Identify the blood parasite species.
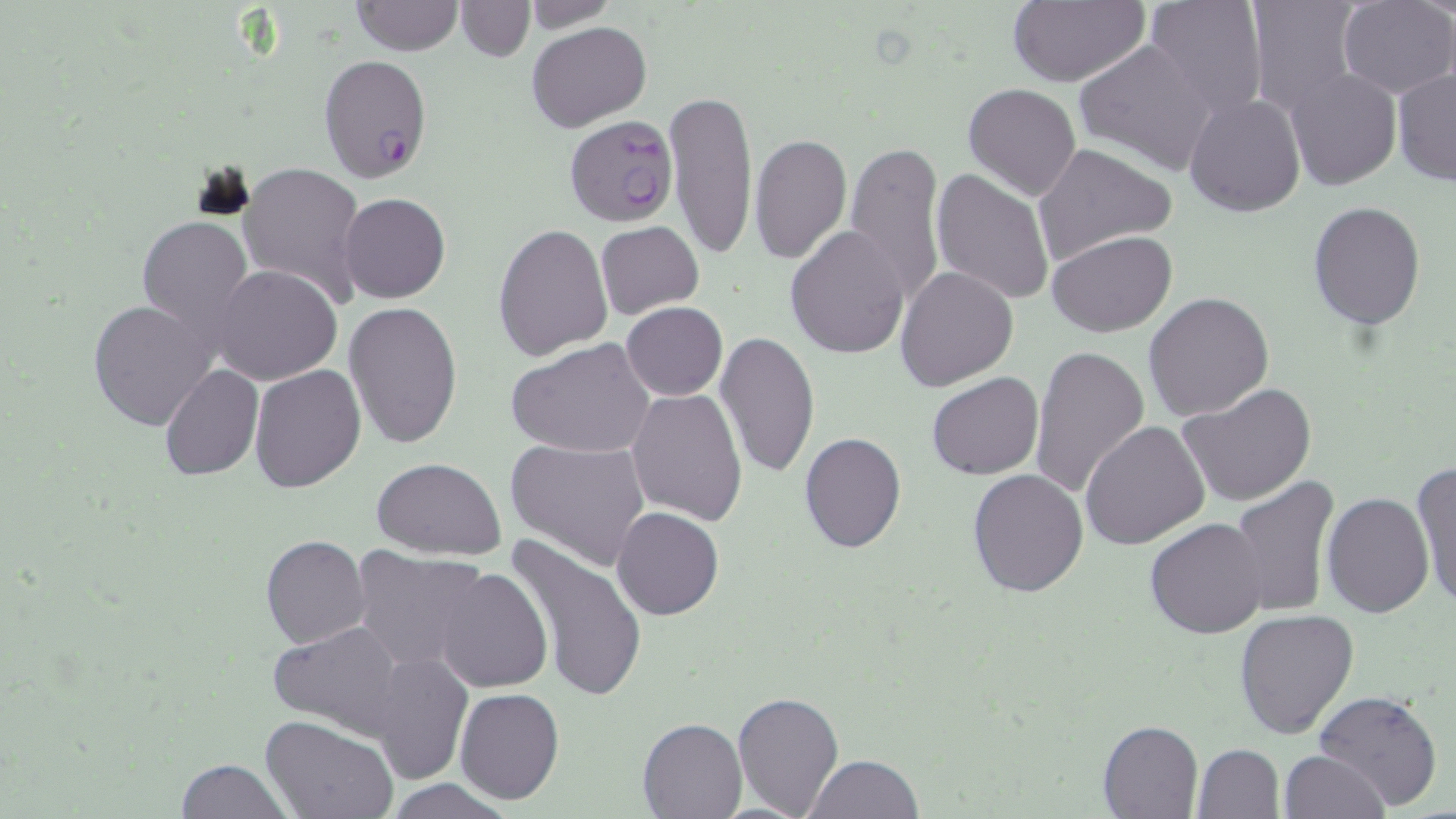

Plasmodium falciparum.

Summary:
  - Coordinate format: approximate bounding boxes as named x1/y1/x2/y2 corners in pixels
  - Uninfected red blood cell locations: (x1=454, y1=0, x2=535, y2=61), (x1=522, y1=0, x2=618, y2=33), (x1=1006, y1=0, x2=1150, y2=87), (x1=1143, y1=0, x2=1270, y2=118), (x1=1245, y1=0, x2=1362, y2=115), (x1=1337, y1=0, x2=1455, y2=98), (x1=351, y1=1, x2=463, y2=55), (x1=527, y1=20, x2=651, y2=131), (x1=1074, y1=38, x2=1219, y2=178), (x1=1286, y1=68, x2=1400, y2=190), (x1=1392, y1=69, x2=1456, y2=188), (x1=963, y1=82, x2=1081, y2=201), (x1=664, y1=88, x2=758, y2=259), (x1=1184, y1=93, x2=1307, y2=218), (x1=750, y1=131, x2=852, y2=265), (x1=845, y1=141, x2=944, y2=307), (x1=1032, y1=143, x2=1176, y2=269), (x1=237, y1=161, x2=366, y2=308), (x1=930, y1=169, x2=1055, y2=305), (x1=340, y1=193, x2=450, y2=302), (x1=1307, y1=201, x2=1426, y2=328), (x1=136, y1=213, x2=254, y2=351), (x1=595, y1=222, x2=704, y2=318), (x1=493, y1=223, x2=614, y2=360), (x1=785, y1=225, x2=910, y2=359), (x1=1047, y1=230, x2=1177, y2=338), (x1=212, y1=263, x2=343, y2=386), (x1=895, y1=266, x2=1017, y2=391), (x1=1144, y1=292, x2=1274, y2=422), (x1=87, y1=298, x2=215, y2=429), (x1=344, y1=301, x2=464, y2=451), (x1=621, y1=302, x2=728, y2=400), (x1=716, y1=330, x2=821, y2=478), (x1=508, y1=339, x2=655, y2=459), (x1=1027, y1=342, x2=1148, y2=501), (x1=159, y1=364, x2=263, y2=481), (x1=249, y1=365, x2=366, y2=493), (x1=926, y1=372, x2=1044, y2=480), (x1=1177, y1=382, x2=1319, y2=506), (x1=627, y1=390, x2=747, y2=524), (x1=1080, y1=420, x2=1209, y2=549), (x1=799, y1=432, x2=907, y2=553), (x1=506, y1=438, x2=652, y2=571), (x1=372, y1=458, x2=507, y2=559), (x1=1412, y1=463, x2=1456, y2=609), (x1=968, y1=468, x2=1088, y2=596), (x1=1229, y1=477, x2=1341, y2=619), (x1=1321, y1=492, x2=1434, y2=618), (x1=612, y1=507, x2=724, y2=620), (x1=1143, y1=517, x2=1271, y2=639), (x1=260, y1=535, x2=371, y2=650), (x1=505, y1=535, x2=651, y2=703), (x1=350, y1=546, x2=490, y2=673), (x1=432, y1=566, x2=553, y2=693), (x1=1234, y1=608, x2=1361, y2=740), (x1=266, y1=620, x2=408, y2=740), (x1=371, y1=650, x2=473, y2=783), (x1=1313, y1=687, x2=1443, y2=814), (x1=455, y1=688, x2=565, y2=805), (x1=732, y1=690, x2=845, y2=818), (x1=260, y1=715, x2=399, y2=819), (x1=638, y1=717, x2=746, y2=818), (x1=1097, y1=719, x2=1203, y2=818), (x1=1192, y1=743, x2=1285, y2=818), (x1=1279, y1=749, x2=1388, y2=819), (x1=805, y1=754, x2=925, y2=818), (x1=176, y1=757, x2=289, y2=819), (x1=385, y1=779, x2=515, y2=818)
  - Plasmodium falciparum-infected red blood cell locations: (x1=318, y1=54, x2=431, y2=181), (x1=568, y1=115, x2=683, y2=228)
  - Modality: light microscopy
  - Image size: 1456×819 pixels
  - Field of view: single
  - Magnification: 1000x
  - Preparation: thin blood film
  - Stain: May-Grünwald-Giemsa